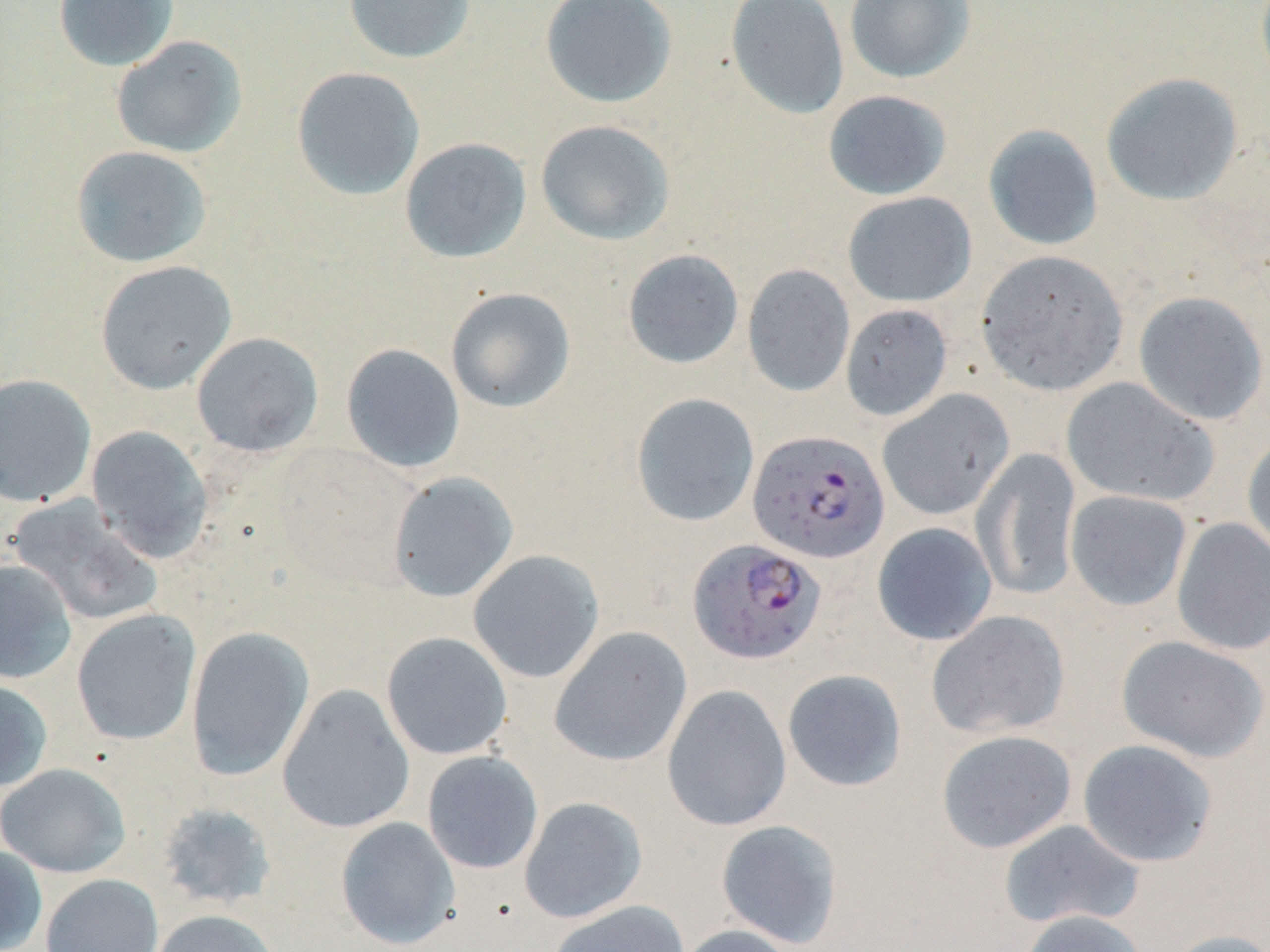
Summary:
  - Coordinate format: approximate bounding boxes as (x1, y1, x2, y2) in pixels
  - Plasmodium falciparum-infected red blood cell locations: (747, 429, 890, 563), (687, 537, 827, 665)
  - Uninfected red blood cell locations: (52, 0, 180, 71), (343, 0, 476, 64), (540, 0, 677, 108), (725, 0, 849, 120), (844, 0, 975, 84), (111, 35, 248, 159), (291, 67, 425, 201), (1101, 72, 1243, 206), (822, 89, 952, 201), (535, 120, 675, 245), (982, 124, 1103, 251), (399, 138, 532, 263), (71, 145, 213, 268), (842, 192, 976, 307), (622, 249, 744, 369), (976, 250, 1129, 396), (95, 260, 237, 394), (742, 264, 855, 397), (445, 287, 576, 413), (1133, 290, 1269, 426), (840, 304, 953, 421), (191, 332, 324, 457), (341, 343, 465, 474), (0, 373, 97, 508), (1061, 377, 1218, 507), (877, 389, 1015, 521), (630, 392, 760, 527), (86, 425, 213, 563), (1242, 434, 1270, 561), (972, 447, 1082, 601), (388, 472, 518, 602), (1065, 490, 1192, 612), (7, 495, 164, 626), (1171, 516, 1270, 655), (871, 522, 997, 646), (468, 550, 605, 684), (0, 559, 77, 684), (71, 610, 201, 746), (926, 610, 1070, 740), (186, 626, 314, 781), (549, 626, 692, 767), (381, 632, 513, 760), (1116, 635, 1269, 762), (782, 669, 907, 792), (0, 677, 52, 792), (277, 684, 415, 833), (662, 685, 792, 831), (936, 729, 1077, 853), (1077, 738, 1218, 867), (422, 751, 544, 874), (1, 763, 131, 877), (519, 796, 647, 924), (155, 802, 278, 910), (336, 817, 460, 950), (716, 819, 844, 948), (998, 819, 1146, 931), (0, 844, 47, 952), (40, 873, 163, 952), (547, 900, 690, 951), (150, 909, 279, 952), (1015, 909, 1150, 952), (674, 924, 800, 952), (1163, 929, 1270, 952)
  - Slide-level diagnosis: Plasmodium falciparum
  - Stain: May-Grünwald-Giemsa
  - Magnification: 1000x
  - Field of view: one of a larger specimen
  - Image size: 1270×952 pixels
  - Modality: optical microscopy
  - Preparation: thin blood film